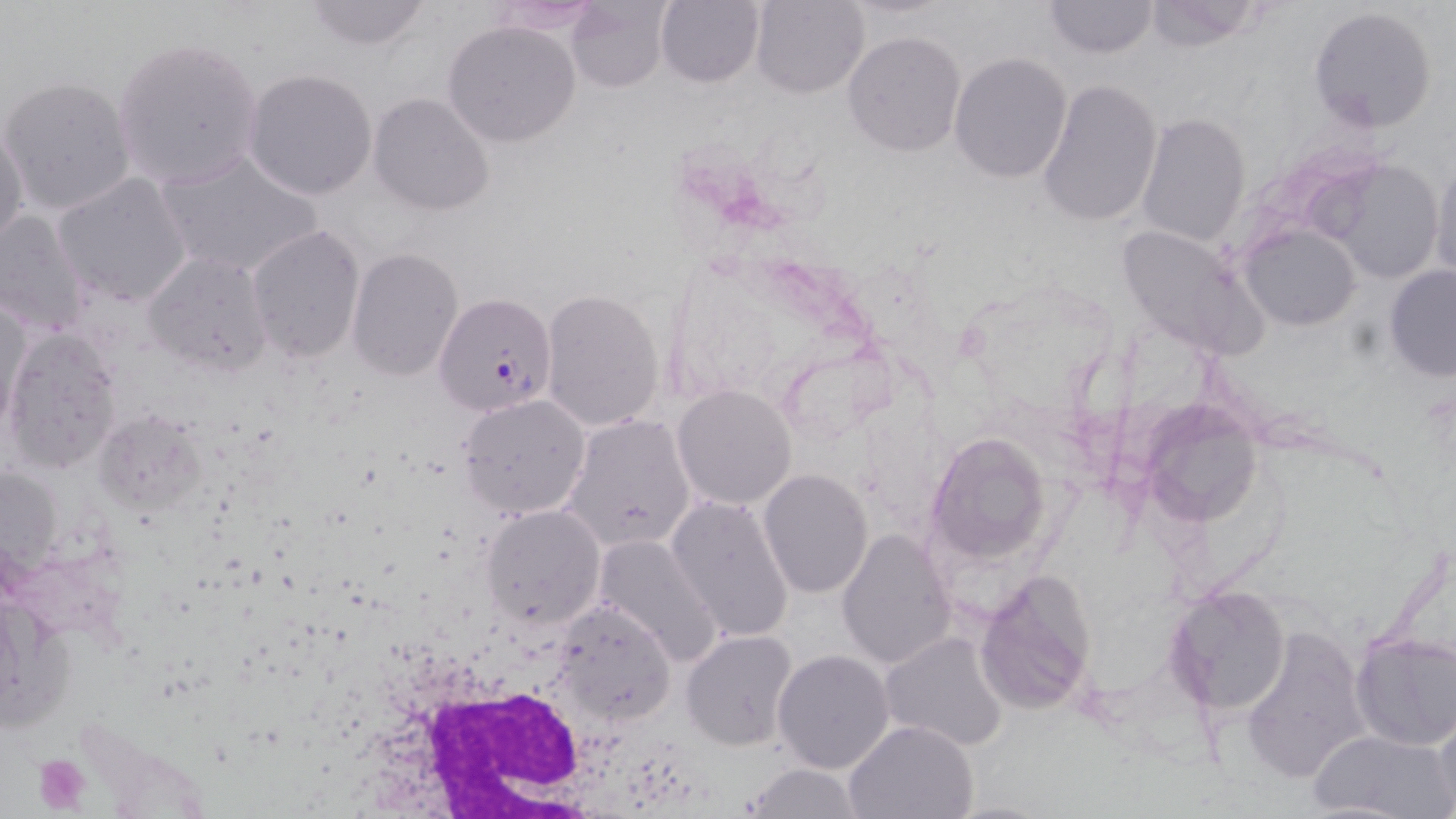
Summary:
  - Coordinate format: approximate bounding boxes as (x1,y1)-(x2,y2) corner pairs in pixels
  - Uninfected red blood cell locations: (297,0)-(435,50), (749,0)-(869,98), (1140,0)-(1270,51), (654,1)-(765,88), (1042,1)-(1159,59), (565,2)-(673,91), (1307,6)-(1438,133), (444,20)-(581,147), (843,31)-(965,156), (111,36)-(265,190), (949,52)-(1073,183), (244,68)-(378,200), (1,75)-(137,216), (1038,78)-(1163,230), (368,92)-(495,215), (1136,112)-(1251,247), (0,123)-(30,252), (154,149)-(322,279), (1429,157)-(1455,282), (1321,158)-(1447,284), (53,172)-(193,308), (0,210)-(91,336), (245,224)-(366,363), (1241,224)-(1361,330), (1115,225)-(1266,357), (345,247)-(465,380), (141,250)-(272,375), (1384,265)-(1456,381), (541,290)-(666,434), (2,293)-(33,434), (3,329)-(123,471), (671,385)-(797,509), (457,392)-(591,519), (1140,394)-(1263,528), (95,412)-(207,515), (563,415)-(697,553), (926,432)-(1058,564), (757,468)-(874,598), (667,493)-(798,645), (480,504)-(605,628), (838,528)-(955,669), (595,533)-(724,669), (976,569)-(1099,715), (1162,585)-(1292,716), (549,597)-(677,728), (1239,623)-(1372,785), (682,630)-(798,749), (880,630)-(1008,753), (1349,630)-(1456,751), (771,649)-(894,775), (1431,710)-(1456,816), (844,719)-(979,819), (1306,728)-(1451,817), (742,763)-(865,819)
  - Plasmodium falciparum-infected red blood cell locations: (436,287)-(574,414)
  - Platelet locations: (32,754)-(91,812)
  - White blood cell locations: (401,673)-(657,819)
  - Slide-level diagnosis: Plasmodium falciparum
  - Field of view: one of a larger specimen
  - Stain: May-Grünwald-Giemsa
  - Modality: light microscopy
  - Magnification: 1000x
  - Preparation: thin blood film
  - Image size: 1456×819 pixels